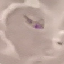
{
  "result": "malaria parasites identified",
  "stain": "Giemsa",
  "preparation": "thin blood smear",
  "image_type": "cell patch, automatically extracted from a larger field of view and resized to 64 × 64 pixels",
  "capture": "smartphone through the microscope eyepiece"
}